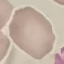

malaria status = uninfected
stain = Giemsa
capture = smartphone through the microscope eyepiece
image type = automatically extracted cell patch, resized to 64 × 64 pixels
preparation = thin smear